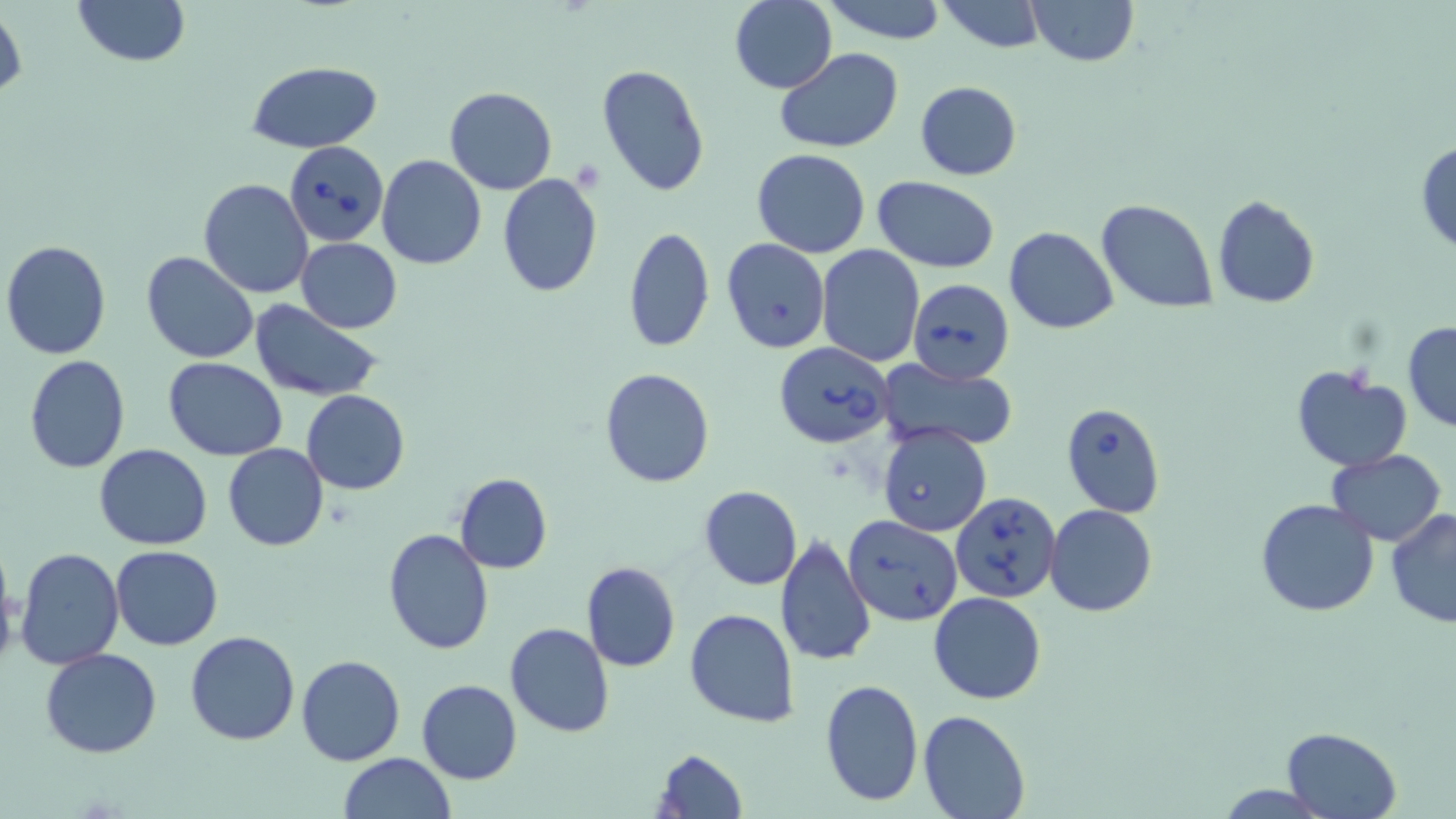
slide-level diagnosis = Babesia divergens
magnification = 1000x
preparation = thin blood film
uninfected red blood cell locations = approximate bounding boxes as named x1/y1/x2/y2 corners in pixels: (x1=72, y1=0, x2=191, y2=67), (x1=822, y1=0, x2=949, y2=44), (x1=937, y1=0, x2=1049, y2=53), (x1=1025, y1=0, x2=1141, y2=67), (x1=729, y1=1, x2=838, y2=92), (x1=1, y1=3, x2=25, y2=108), (x1=774, y1=48, x2=904, y2=153), (x1=246, y1=60, x2=384, y2=155), (x1=595, y1=64, x2=710, y2=196), (x1=914, y1=81, x2=1023, y2=181), (x1=444, y1=86, x2=558, y2=194), (x1=1415, y1=140, x2=1456, y2=256), (x1=751, y1=149, x2=871, y2=258), (x1=376, y1=155, x2=488, y2=271), (x1=498, y1=172, x2=602, y2=295), (x1=872, y1=176, x2=999, y2=271), (x1=198, y1=178, x2=312, y2=299), (x1=1212, y1=195, x2=1321, y2=308), (x1=1095, y1=199, x2=1218, y2=312), (x1=624, y1=226, x2=715, y2=354), (x1=1005, y1=227, x2=1118, y2=333), (x1=296, y1=236, x2=402, y2=333), (x1=721, y1=239, x2=830, y2=353), (x1=1, y1=240, x2=112, y2=359), (x1=816, y1=245, x2=924, y2=366), (x1=141, y1=252, x2=260, y2=363), (x1=249, y1=301, x2=383, y2=402), (x1=1402, y1=322, x2=1456, y2=432), (x1=24, y1=356, x2=130, y2=474), (x1=163, y1=357, x2=287, y2=460), (x1=878, y1=359, x2=1019, y2=451), (x1=1291, y1=365, x2=1412, y2=473), (x1=598, y1=367, x2=715, y2=488), (x1=301, y1=389, x2=409, y2=494), (x1=222, y1=443, x2=329, y2=551), (x1=95, y1=444, x2=212, y2=549), (x1=1326, y1=448, x2=1446, y2=545), (x1=455, y1=472, x2=552, y2=574), (x1=698, y1=484, x2=802, y2=590), (x1=1257, y1=499, x2=1381, y2=618), (x1=1045, y1=505, x2=1158, y2=617), (x1=1386, y1=508, x2=1456, y2=630), (x1=383, y1=528, x2=494, y2=655), (x1=776, y1=535, x2=876, y2=667), (x1=111, y1=545, x2=224, y2=650), (x1=14, y1=547, x2=125, y2=669), (x1=581, y1=561, x2=680, y2=673), (x1=0, y1=566, x2=21, y2=673), (x1=928, y1=592, x2=1045, y2=704), (x1=684, y1=608, x2=801, y2=729), (x1=505, y1=623, x2=614, y2=737), (x1=185, y1=630, x2=301, y2=746), (x1=41, y1=649, x2=162, y2=759), (x1=296, y1=655, x2=405, y2=766), (x1=819, y1=677, x2=923, y2=807), (x1=415, y1=679, x2=522, y2=785), (x1=918, y1=708, x2=1030, y2=819), (x1=1281, y1=726, x2=1402, y2=819), (x1=652, y1=746, x2=748, y2=819), (x1=339, y1=752, x2=456, y2=818)
modality = optical microscopy
field of view = one of a larger specimen
image size = 1456×819 pixels
Babesia divergens-infected red blood cell locations = approximate bounding boxes as named x1/y1/x2/y2 corners in pixels: (x1=285, y1=141, x2=389, y2=246), (x1=907, y1=278, x2=1015, y2=386), (x1=772, y1=342, x2=893, y2=450), (x1=1060, y1=401, x2=1166, y2=517), (x1=878, y1=425, x2=992, y2=536), (x1=952, y1=492, x2=1060, y2=603), (x1=844, y1=513, x2=962, y2=627)
stain = May-Grünwald-Giemsa